State the preparation type.
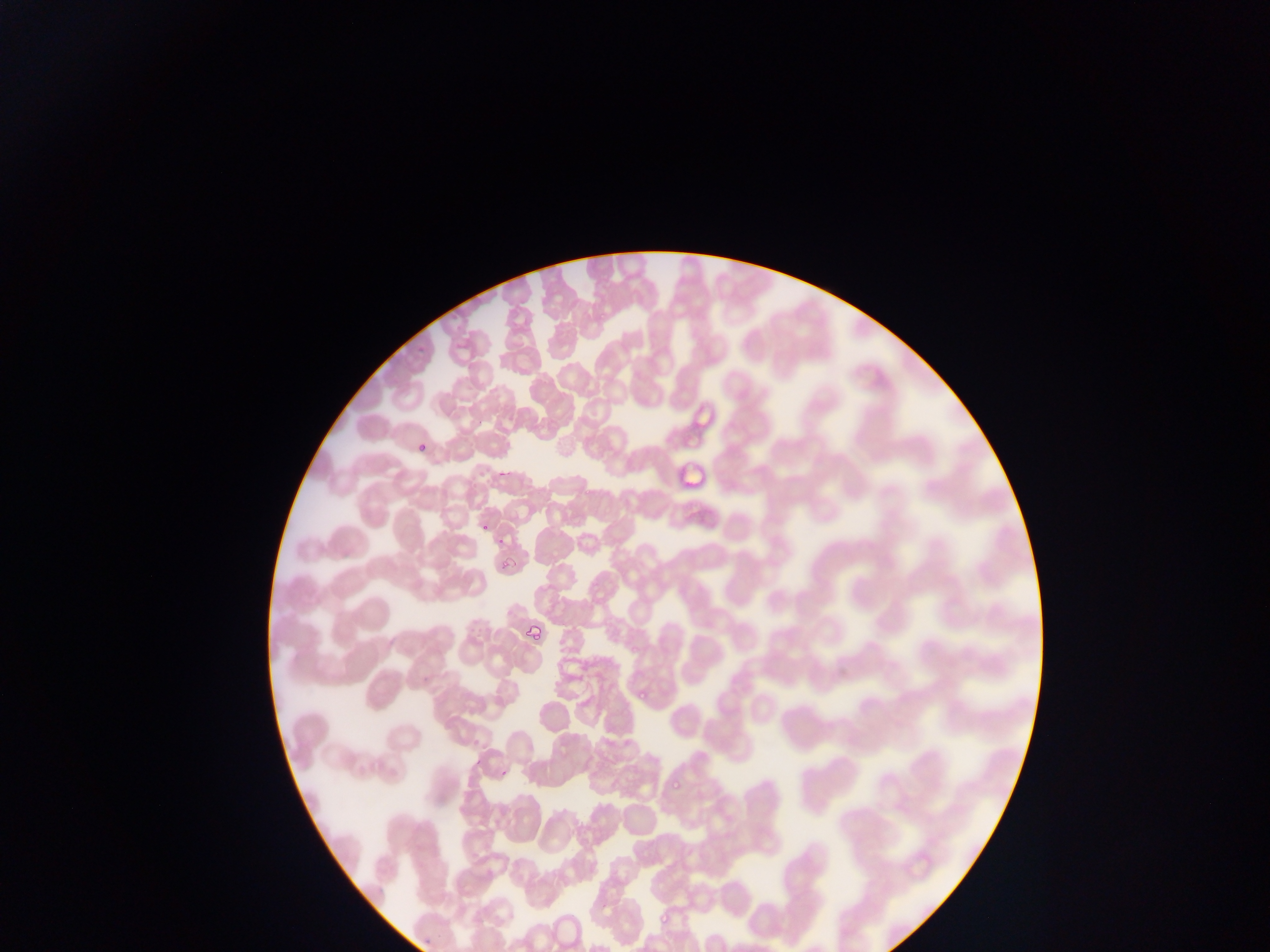

This is a thin smear.

Approximate bounding boxes as [left, top, right, bottom] in pixels.
Summary:
  - Malaria parasite locations: [689, 406, 721, 430], [680, 429, 706, 446], [414, 445, 429, 455], [499, 467, 510, 480], [679, 467, 707, 485], [477, 518, 498, 537], [496, 533, 507, 544], [496, 556, 515, 580], [523, 619, 540, 639], [626, 638, 639, 650], [636, 687, 649, 701], [474, 759, 481, 770], [502, 769, 508, 780], [672, 778, 684, 792], [654, 907, 669, 927], [424, 938, 432, 945]
  - Country: Ghana
  - Capture: mobile-phone photograph through a microscope
  - Image size: 1270×952 pixels
  - Field of view: single